Give the extent of all Plasmodium malariae-infected red blood cells.
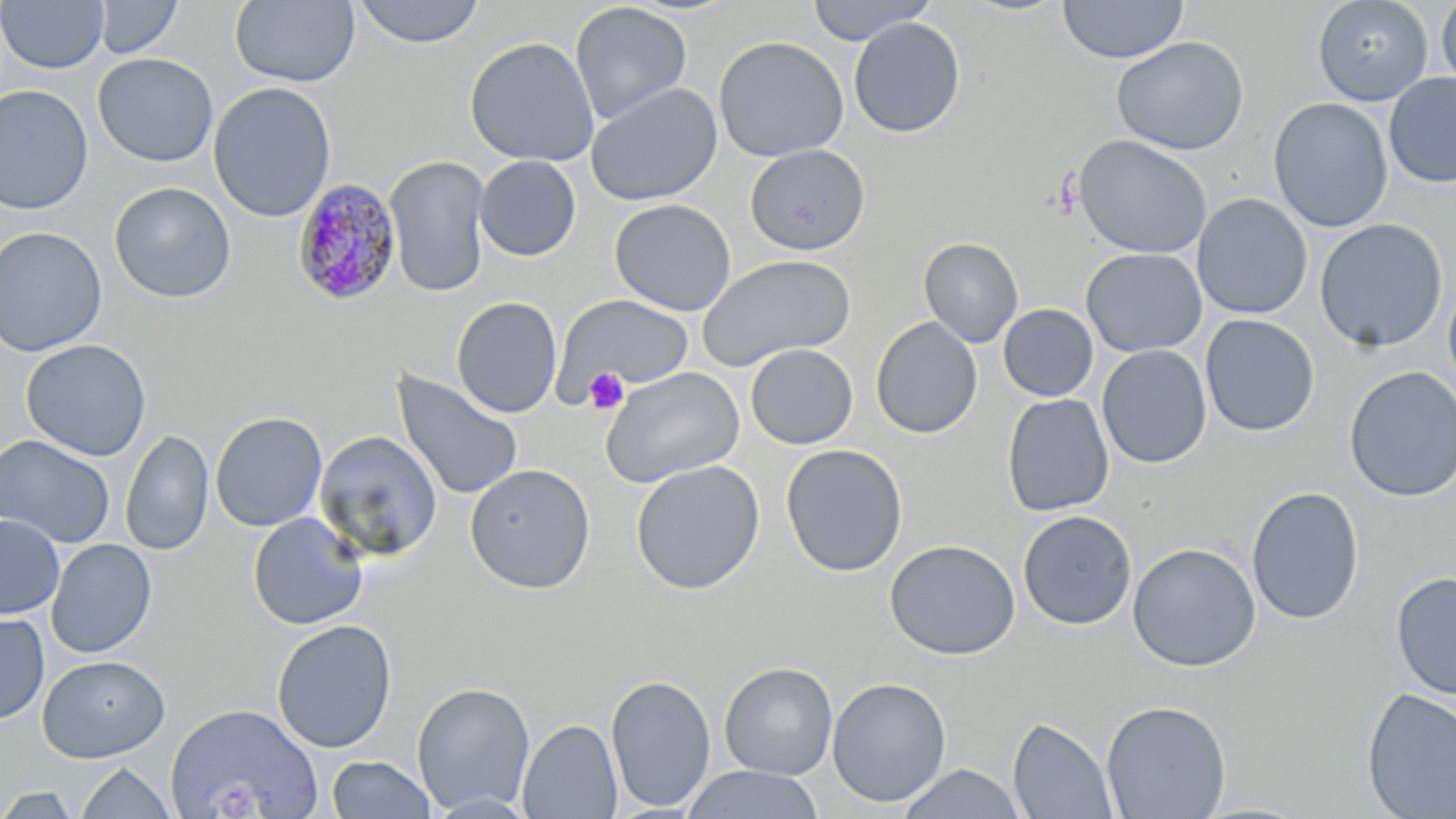

Approximate bounding boxes as named x1/y1/x2/y2 corners in pixels.
Plasmodium malariae-infected red blood cells: (x1=292, y1=178, x2=402, y2=305).

Platelet locations: (x1=583, y1=367, x2=630, y2=415). Uninfected red blood cell locations: (x1=93, y1=0, x2=183, y2=59), (x1=230, y1=0, x2=360, y2=87), (x1=351, y1=0, x2=486, y2=49), (x1=804, y1=0, x2=936, y2=45), (x1=1057, y1=0, x2=1188, y2=64), (x1=1311, y1=0, x2=1434, y2=106), (x1=1436, y1=0, x2=1456, y2=96), (x1=0, y1=1, x2=108, y2=73), (x1=569, y1=2, x2=692, y2=126), (x1=848, y1=17, x2=966, y2=138), (x1=463, y1=36, x2=600, y2=167), (x1=713, y1=36, x2=849, y2=162), (x1=1111, y1=36, x2=1249, y2=155), (x1=92, y1=53, x2=218, y2=167), (x1=1383, y1=73, x2=1456, y2=188), (x1=208, y1=82, x2=337, y2=222), (x1=585, y1=82, x2=723, y2=206), (x1=0, y1=85, x2=94, y2=214), (x1=1267, y1=97, x2=1394, y2=233), (x1=1073, y1=134, x2=1212, y2=259), (x1=744, y1=144, x2=870, y2=255), (x1=474, y1=155, x2=581, y2=261), (x1=384, y1=156, x2=490, y2=297), (x1=109, y1=181, x2=236, y2=303), (x1=1192, y1=194, x2=1312, y2=320), (x1=609, y1=199, x2=736, y2=316), (x1=1313, y1=218, x2=1448, y2=353), (x1=0, y1=226, x2=107, y2=357), (x1=918, y1=237, x2=1023, y2=347), (x1=1081, y1=248, x2=1207, y2=357), (x1=696, y1=254, x2=855, y2=372), (x1=1442, y1=277, x2=1456, y2=398), (x1=555, y1=293, x2=696, y2=392), (x1=451, y1=297, x2=563, y2=418), (x1=998, y1=304, x2=1098, y2=402), (x1=1199, y1=314, x2=1320, y2=437), (x1=870, y1=317, x2=982, y2=439), (x1=20, y1=338, x2=152, y2=461), (x1=745, y1=344, x2=858, y2=449), (x1=1096, y1=344, x2=1212, y2=469), (x1=599, y1=366, x2=745, y2=488), (x1=1343, y1=366, x2=1456, y2=503), (x1=390, y1=369, x2=524, y2=503), (x1=1002, y1=394, x2=1114, y2=517), (x1=210, y1=411, x2=327, y2=532), (x1=121, y1=429, x2=214, y2=556), (x1=314, y1=431, x2=443, y2=564), (x1=1, y1=434, x2=116, y2=548), (x1=780, y1=444, x2=908, y2=578), (x1=630, y1=460, x2=765, y2=595), (x1=464, y1=463, x2=596, y2=595), (x1=1245, y1=486, x2=1364, y2=625), (x1=1017, y1=510, x2=1137, y2=630), (x1=247, y1=512, x2=369, y2=630), (x1=0, y1=515, x2=65, y2=619), (x1=46, y1=538, x2=157, y2=658), (x1=883, y1=539, x2=1021, y2=660), (x1=1127, y1=542, x2=1261, y2=672), (x1=1390, y1=570, x2=1456, y2=701), (x1=0, y1=611, x2=49, y2=725), (x1=271, y1=619, x2=397, y2=753), (x1=37, y1=654, x2=170, y2=763), (x1=718, y1=662, x2=838, y2=780), (x1=605, y1=674, x2=716, y2=812), (x1=826, y1=677, x2=952, y2=807), (x1=411, y1=681, x2=536, y2=815), (x1=1361, y1=688, x2=1456, y2=818), (x1=1101, y1=699, x2=1232, y2=818), (x1=165, y1=702, x2=323, y2=819), (x1=1007, y1=716, x2=1118, y2=818), (x1=516, y1=719, x2=623, y2=818), (x1=326, y1=755, x2=436, y2=818), (x1=74, y1=761, x2=176, y2=818), (x1=896, y1=764, x2=1026, y2=819), (x1=679, y1=765, x2=825, y2=819), (x1=0, y1=786, x2=83, y2=818). Slide-level diagnosis: Plasmodium malariae. Captured at 1000x magnification. Light microscopy. Image is 1456×819 pixels. Thin blood smear. May-Grünwald-Giemsa stain. One field of a larger specimen.